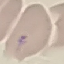

Summary:
  - Result: no malaria parasites detected
  - Image type: automatically extracted cell patch, resized to 64 × 64 pixels
  - Stain: Giemsa
  - Preparation: thin blood film
  - Capture: smartphone through the microscope eyepiece